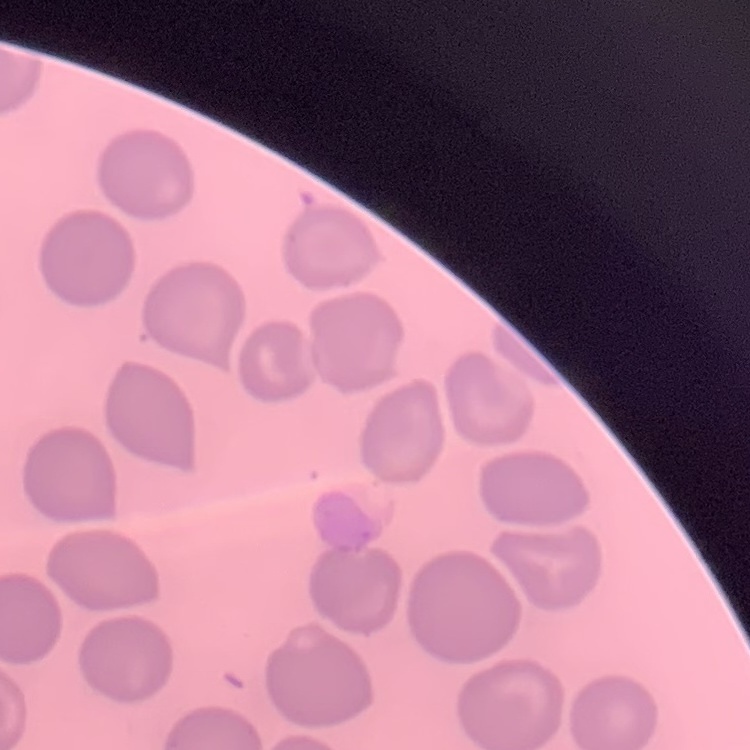

erythrocyte morphology = no rouleaux formation
preparation = thin blood smear
stain = Field's or Giemsa
image type = one tile cut from a larger photomicrograph